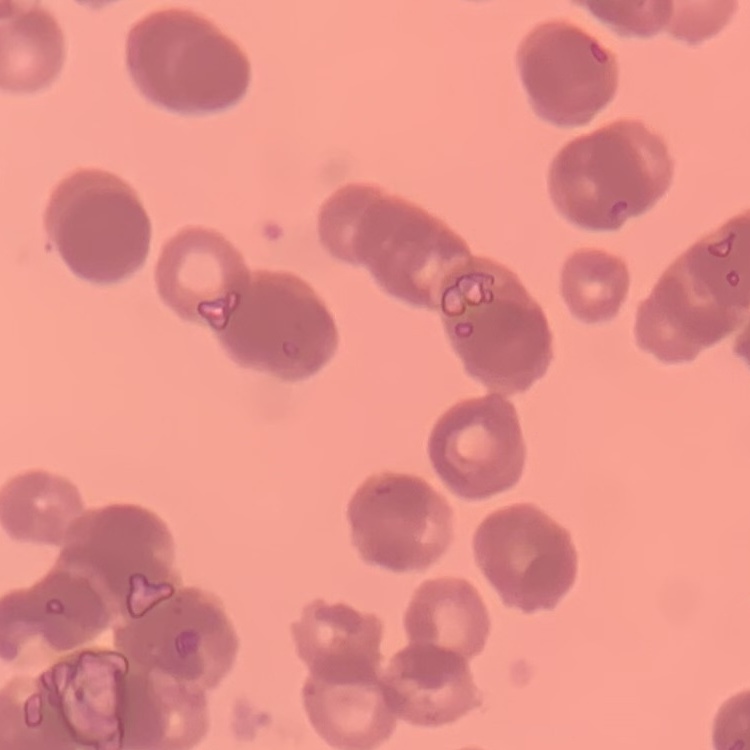
The erythrocytes show rouleaux formation. Thin blood smear. One tile cut from a larger photomicrograph. Field's or Giemsa stain.